Locate and identify every blood parasite.
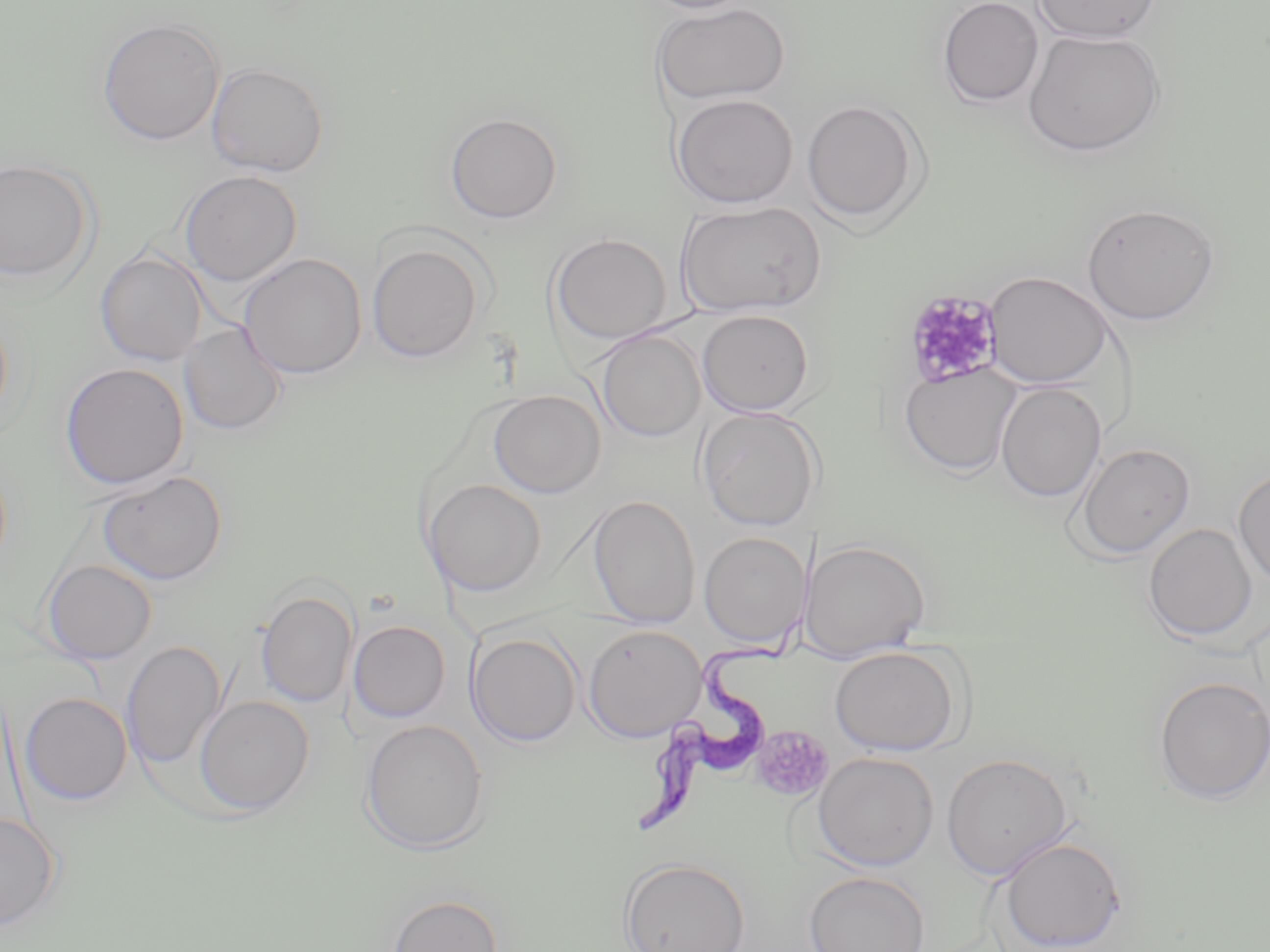
Approximate bounding boxes as (x1,y1)-(x2,y2) corner pairs in pixels.
Trypanosoma brucei: (629,620)-(802,841).
No Plasmodium falciparum, Plasmodium ovale, Plasmodium malariae, Plasmodium vivax, or Babesia divergens observed.

slide-level diagnosis = Trypanosoma brucei
field of view = single
modality = light microscopy
stain = May-Grünwald-Giemsa
image size = 1270×952 pixels
uninfected red blood cell locations = approximate bounding boxes as (x1,y1)-(x2,y2) corner pairs in pixels: (639,0)-(755,14), (937,0)-(1044,108), (1031,0)-(1162,44), (651,2)-(791,106), (96,17)-(226,146), (1022,28)-(1166,158), (206,61)-(329,177), (670,93)-(799,209), (800,98)-(924,226), (444,111)-(563,224), (0,158)-(96,284), (179,170)-(302,286), (675,200)-(827,319), (1082,202)-(1221,326), (550,232)-(672,344), (366,240)-(485,363), (95,250)-(208,366), (238,253)-(368,379), (983,271)-(1113,388), (0,309)-(13,431), (697,309)-(814,416), (178,322)-(287,436), (595,329)-(706,443), (59,362)-(190,491), (899,362)-(1021,477), (995,383)-(1106,502), (488,389)-(606,498), (697,406)-(821,531), (1073,442)-(1196,560), (1233,466)-(1270,587), (98,470)-(228,585), (423,479)-(547,596), (588,494)-(701,628), (1143,523)-(1258,643), (699,532)-(810,648), (802,538)-(931,660), (42,560)-(157,664), (255,588)-(358,707), (348,619)-(451,723), (583,624)-(706,742), (465,630)-(581,747), (122,639)-(226,770), (829,644)-(964,756), (1152,676)-(1269,804), (19,691)-(133,805), (195,695)-(315,815), (359,718)-(490,854), (812,751)-(939,871), (941,752)-(1073,880), (0,810)-(61,931), (997,835)-(1128,951), (618,857)-(750,952), (804,871)-(930,952), (386,892)-(503,952)
preparation = thin blood smear
platelet locations = approximate bounding boxes as (x1,y1)-(x2,y2) corner pairs in pixels: (903,289)-(1005,388), (750,726)-(833,803)
magnification = 1000x